Classify this cell by malaria status.
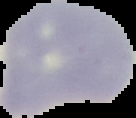

Uninfected.

image type = segmented cell region on a black background
preparation = thin blood film
image size = 136×118 pixels